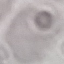

Summary:
  - Malaria status: uninfected
  - Image type: automatically extracted cell patch, resized to 64 × 64 pixels
  - Capture: smartphone through the microscope eyepiece
  - Preparation: thin smear
  - Stain: Giemsa